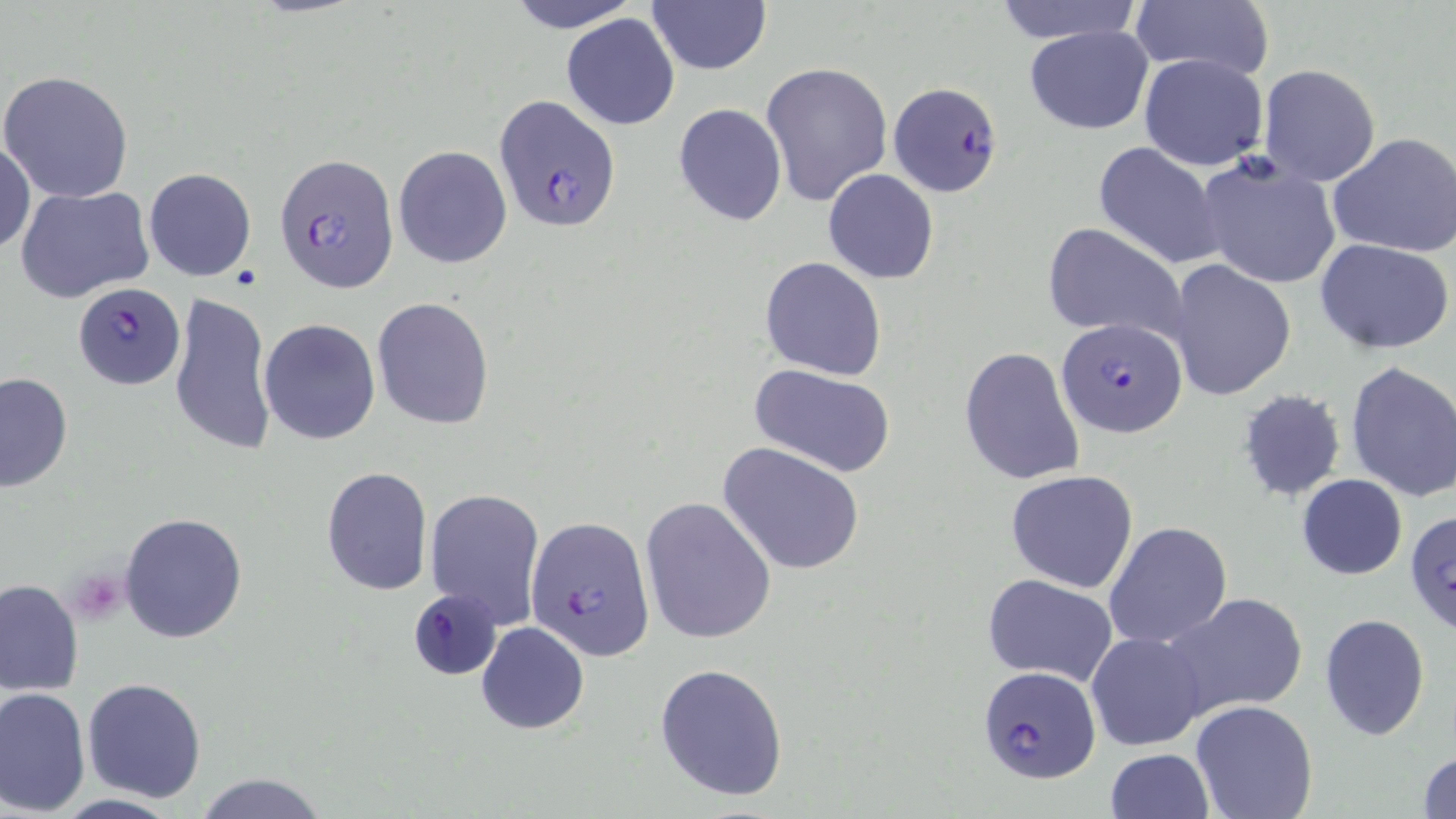

Approximate bounding boxes as (x1,y1)-(x2,y2) corner pairs in pixels. Uninfected red blood cell locations: (511,0)-(636,33), (992,0)-(1143,44), (647,1)-(771,76), (1129,1)-(1274,83), (562,14)-(679,130), (1024,26)-(1152,134), (1139,53)-(1269,171), (762,61)-(893,206), (1257,64)-(1382,187), (1,69)-(134,202), (673,103)-(787,227), (1328,132)-(1456,260), (0,141)-(35,256), (1093,141)-(1227,270), (394,145)-(512,269), (1194,155)-(1342,289), (143,168)-(256,281), (823,169)-(939,284), (15,184)-(153,303), (1042,224)-(1187,345), (1315,237)-(1454,354), (758,257)-(887,381), (1166,260)-(1297,401), (168,290)-(275,458), (373,297)-(493,431), (259,319)-(381,444), (959,346)-(1085,486), (1345,360)-(1456,503), (751,366)-(896,477), (0,371)-(72,492), (1236,387)-(1348,502), (718,441)-(865,575), (320,466)-(433,596), (1006,470)-(1139,593), (1296,474)-(1407,580), (424,487)-(545,628), (640,496)-(776,644), (1404,506)-(1455,638), (119,512)-(249,645), (1104,520)-(1234,651), (981,572)-(1119,686), (1,579)-(82,696), (409,587)-(502,680), (1160,592)-(1310,720), (1319,613)-(1431,739), (476,622)-(589,734), (1087,631)-(1205,750), (655,662)-(789,801), (82,678)-(208,802), (0,687)-(92,814), (1190,700)-(1320,819), (1105,747)-(1214,818), (1415,749)-(1456,819), (194,772)-(330,819), (51,793)-(185,819). Platelet locations: (70,568)-(129,623). Plasmodium falciparum-infected red blood cell locations: (889,82)-(1002,198), (495,96)-(620,230), (276,153)-(399,292), (72,281)-(183,389), (1055,318)-(1188,439), (526,516)-(655,661), (977,667)-(1103,783). Slide-level diagnosis: Plasmodium falciparum. Light microscopy. Captured at 1000x magnification. Thin blood film. One field of a larger specimen. Image is 1456×819 pixels. May-Grünwald-Giemsa stain.